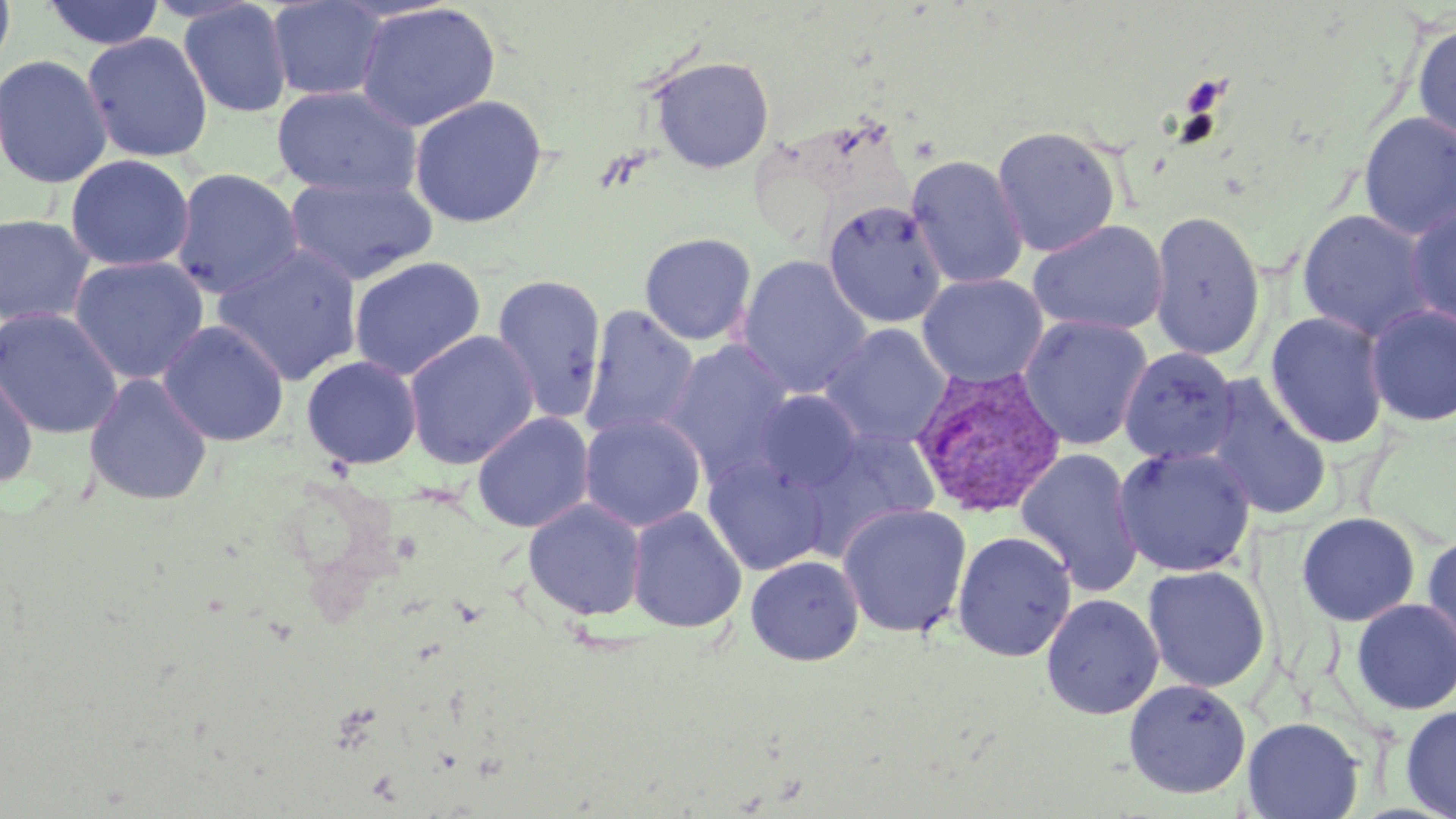

Summary:
  - Coordinate format: approximate bounding boxes as [x1, y1, x2, y2] in pixels
  - Platelet locations: [1180, 75, 1229, 116]
  - Uninfected red blood cell locations: [0, 0, 16, 78], [265, 0, 390, 102], [42, 1, 165, 50], [177, 1, 293, 119], [354, 2, 502, 132], [1412, 22, 1456, 144], [81, 31, 214, 163], [0, 54, 113, 189], [649, 56, 775, 173], [271, 84, 422, 198], [408, 94, 548, 228], [1358, 112, 1456, 240], [991, 126, 1122, 257], [64, 154, 195, 272], [905, 155, 1028, 290], [171, 168, 304, 298], [283, 175, 438, 286], [823, 200, 948, 328], [1404, 202, 1456, 329], [1297, 209, 1435, 343], [1149, 210, 1266, 363], [0, 213, 96, 327], [1028, 219, 1169, 336], [639, 232, 757, 345], [211, 243, 363, 386], [69, 255, 210, 385], [736, 255, 872, 399], [348, 256, 487, 381], [491, 273, 608, 422], [917, 273, 1048, 389], [1365, 304, 1456, 426], [580, 305, 701, 440], [0, 306, 123, 439], [1265, 311, 1389, 449], [1019, 315, 1153, 451], [157, 319, 290, 446], [821, 324, 952, 450], [403, 329, 540, 469], [660, 340, 799, 487], [1119, 347, 1240, 466], [301, 354, 423, 469], [0, 356, 39, 490], [83, 373, 213, 507], [1203, 376, 1333, 522], [752, 390, 864, 495], [472, 412, 594, 533], [579, 413, 706, 532], [795, 426, 941, 559], [1113, 445, 1256, 578], [1015, 448, 1144, 596], [701, 455, 828, 576], [522, 498, 647, 621], [837, 503, 972, 638], [626, 505, 747, 633], [1297, 512, 1420, 626], [952, 530, 1077, 661], [1421, 531, 1456, 667], [745, 555, 865, 666], [1142, 565, 1270, 693], [1041, 593, 1164, 719], [1351, 598, 1456, 715], [1123, 679, 1251, 798], [1399, 705, 1456, 819], [1242, 716, 1363, 819]
  - Plasmodium vivax-infected red blood cell locations: [910, 364, 1066, 519]
  - Slide-level diagnosis: Plasmodium vivax
  - Field of view: single
  - Preparation: thin blood film
  - Stain: May-Grünwald-Giemsa
  - Image size: 1456×819 pixels
  - Magnification: 1000x
  - Modality: light microscopy